Comment on the morphology of the erythrocytes.
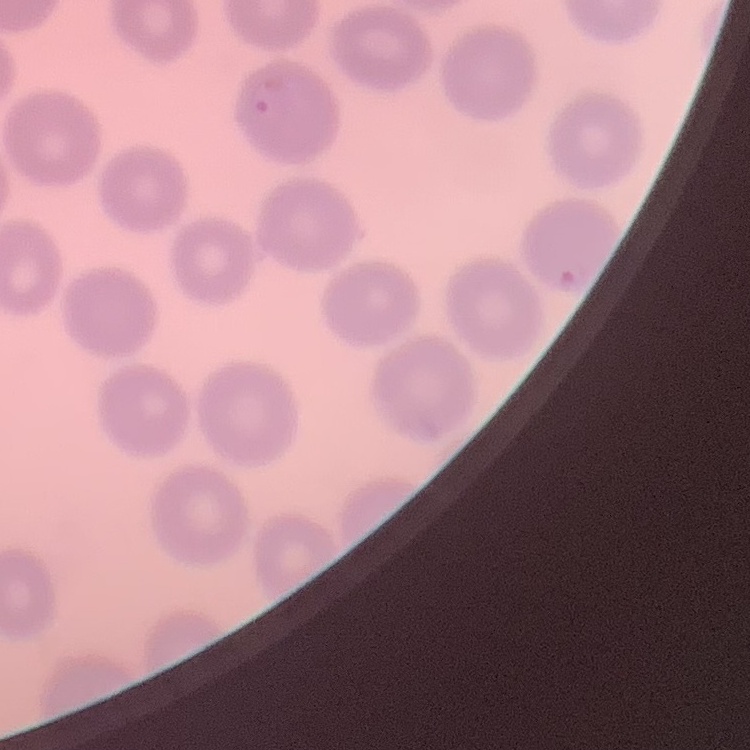
They show no rouleaux formation.

One tile cut from a larger photomicrograph. Field's or Giemsa stain. Thin peripheral smear.